Assess the morphology of the erythrocytes.
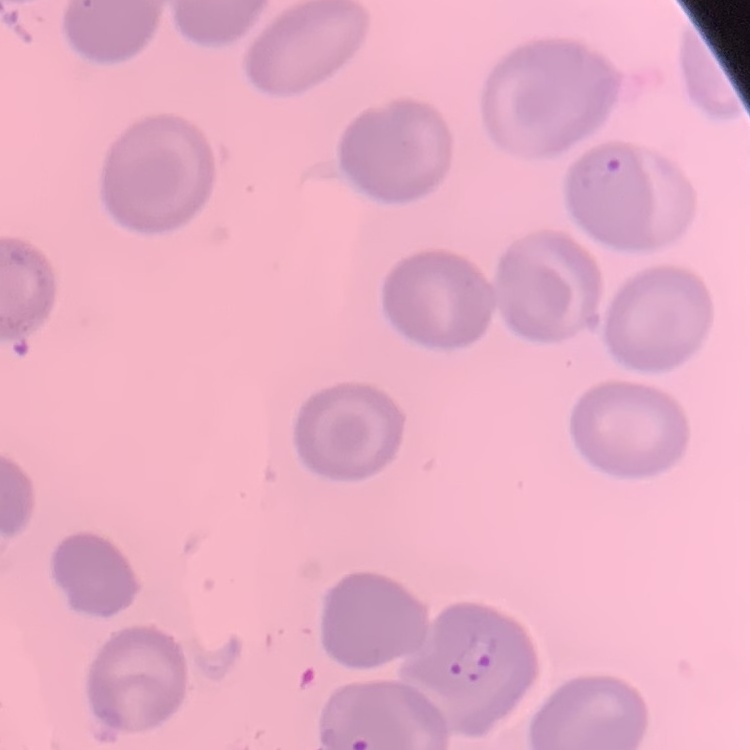

No rouleaux formation.

stain = Field's or Giemsa
image type = square crop of a larger photomicrograph
preparation = thin blood smear